Draw a bounding box around every leukocyte (white blood cell).
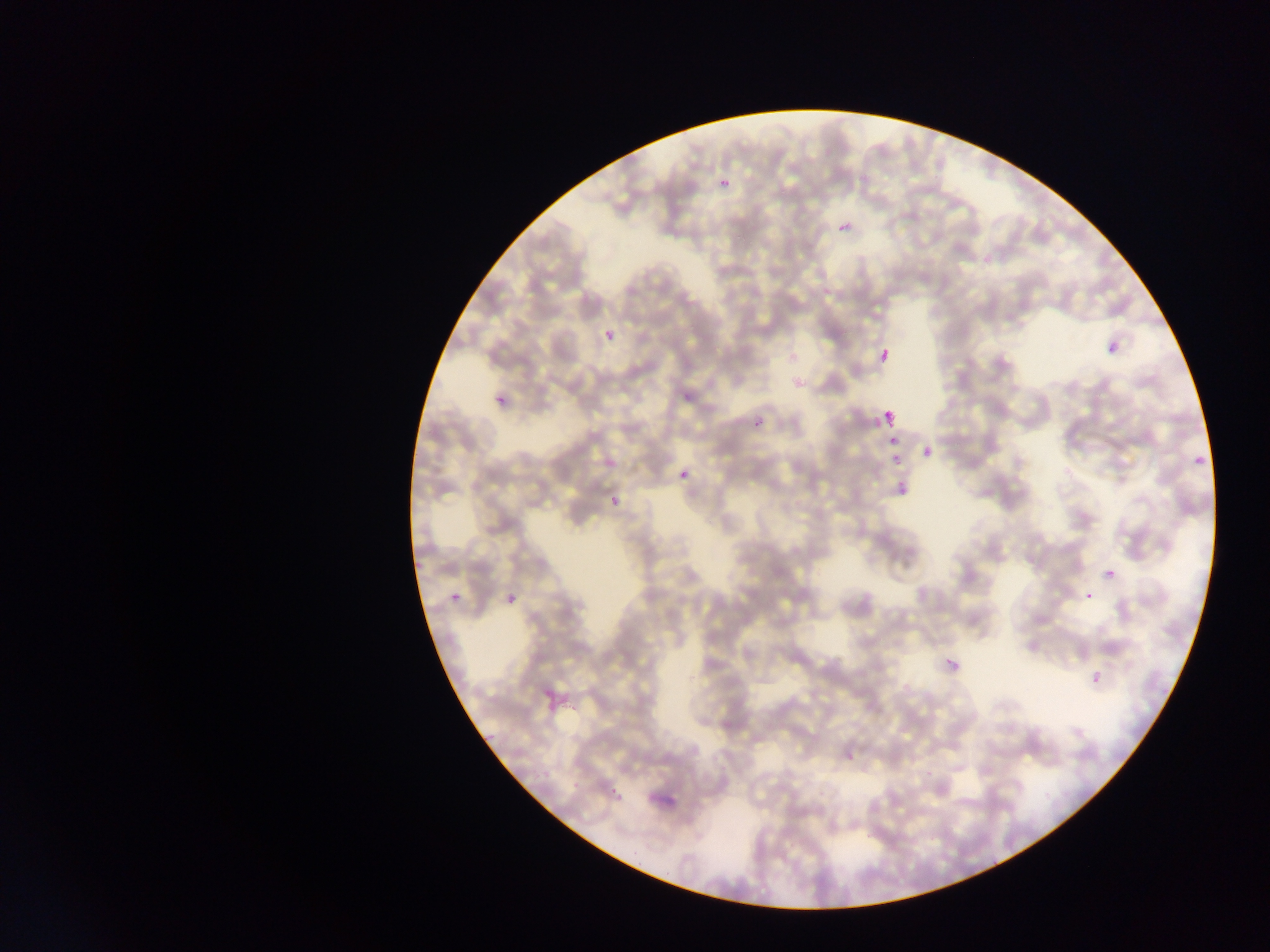
No leukocytes observed.

{
  "field_of_view": "single",
  "preparation": "thin blood smear",
  "malaria_parasite_locations": "approximate bounding boxes as left top right bottom in pixels (subset; some below the resolvable size): 709 170 742 196; 839 221 852 236; 1100 322 1123 358; 603 329 616 344; 875 345 897 370; 485 378 515 421; 879 407 899 430; 749 414 769 435; 885 433 901 450; 920 442 938 462; 1187 447 1210 476; 679 468 691 481; 888 471 913 499; 1103 567 1118 583; 442 578 463 609; 498 580 524 605; 1083 592 1094 603; 938 648 967 681; 1086 666 1108 691",
  "capture": "mobile-phone photograph through a microscope",
  "country": "Ghana",
  "image_size": "1270×952 pixels"
}